State the blood parasite species.
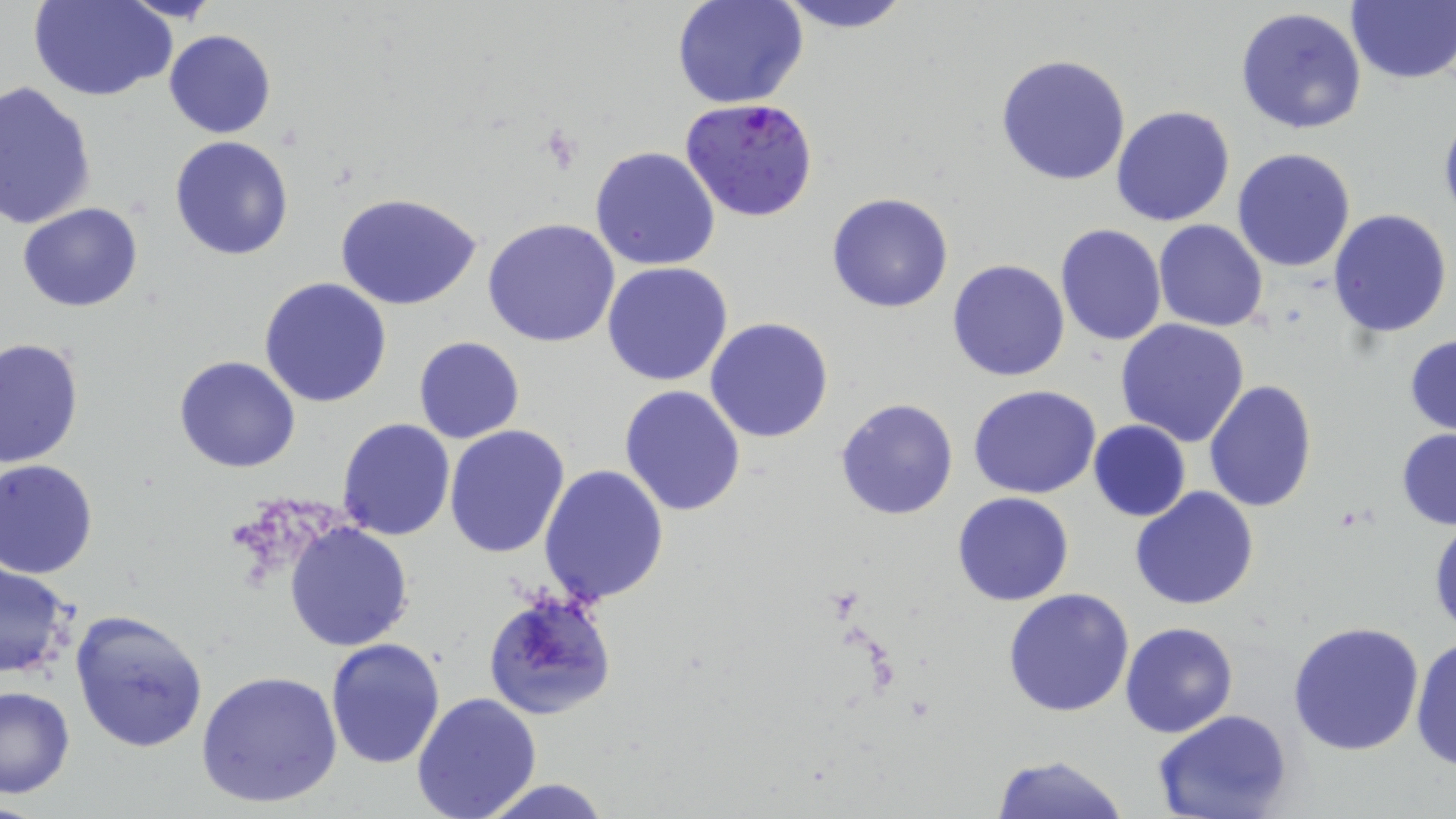
Plasmodium falciparum.

Summary:
  - Coordinate format: approximate bounding boxes as named x1/y1/x2/y2 corners in pixels
  - Plasmodium falciparum-infected red blood cell locations: (x1=682, y1=98, x2=818, y2=222)
  - Uninfected red blood cell locations: (x1=30, y1=0, x2=176, y2=102), (x1=768, y1=0, x2=917, y2=34), (x1=673, y1=1, x2=807, y2=109), (x1=1345, y1=3, x2=1456, y2=85), (x1=1235, y1=7, x2=1367, y2=135), (x1=163, y1=29, x2=277, y2=139), (x1=993, y1=54, x2=1133, y2=187), (x1=0, y1=81, x2=98, y2=231), (x1=1015, y1=81, x2=1235, y2=211), (x1=1110, y1=104, x2=1236, y2=227), (x1=1438, y1=110, x2=1456, y2=231), (x1=169, y1=135, x2=294, y2=260), (x1=589, y1=146, x2=720, y2=271), (x1=1232, y1=147, x2=1357, y2=274), (x1=334, y1=191, x2=484, y2=312), (x1=827, y1=193, x2=952, y2=313), (x1=17, y1=201, x2=145, y2=312), (x1=1328, y1=208, x2=1452, y2=339), (x1=482, y1=218, x2=621, y2=347), (x1=1153, y1=218, x2=1270, y2=332), (x1=1054, y1=223, x2=1167, y2=347), (x1=947, y1=259, x2=1071, y2=382), (x1=603, y1=262, x2=734, y2=386), (x1=258, y1=277, x2=392, y2=408), (x1=705, y1=316, x2=835, y2=444), (x1=1117, y1=318, x2=1250, y2=445), (x1=1405, y1=332, x2=1456, y2=438), (x1=413, y1=335, x2=525, y2=443), (x1=1, y1=337, x2=83, y2=467), (x1=174, y1=354, x2=303, y2=473), (x1=1204, y1=380, x2=1317, y2=514), (x1=619, y1=385, x2=747, y2=518), (x1=969, y1=385, x2=1101, y2=499), (x1=835, y1=397, x2=958, y2=520), (x1=336, y1=418, x2=454, y2=539), (x1=1088, y1=420, x2=1192, y2=520), (x1=443, y1=425, x2=570, y2=559), (x1=1396, y1=429, x2=1456, y2=529), (x1=0, y1=459, x2=99, y2=578), (x1=538, y1=464, x2=669, y2=609), (x1=1129, y1=486, x2=1260, y2=611), (x1=952, y1=491, x2=1075, y2=605), (x1=1428, y1=517, x2=1456, y2=636), (x1=285, y1=521, x2=414, y2=650), (x1=0, y1=558, x2=79, y2=681), (x1=1002, y1=588, x2=1135, y2=717), (x1=483, y1=589, x2=616, y2=721), (x1=68, y1=607, x2=209, y2=754), (x1=1119, y1=621, x2=1239, y2=737), (x1=1287, y1=622, x2=1426, y2=756), (x1=1408, y1=635, x2=1456, y2=773), (x1=325, y1=637, x2=446, y2=768), (x1=196, y1=669, x2=343, y2=809), (x1=0, y1=683, x2=75, y2=798), (x1=410, y1=691, x2=542, y2=819), (x1=1152, y1=711, x2=1293, y2=819), (x1=990, y1=753, x2=1134, y2=819), (x1=471, y1=778, x2=618, y2=819)
  - Preparation: thin blood smear
  - Field of view: one of a larger specimen
  - Stain: May-Grünwald-Giemsa
  - Magnification: 1000x
  - Modality: optical microscopy
  - Image size: 1456×819 pixels